Report the malaria status of this cell.
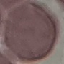
It is uninfected.

Automatically extracted cell patch, resized to 64 × 64 pixels. Thin blood smear. Photographed with a smartphone camera at the microscope eyepiece. Giemsa-stained preparation.